Outline each Plasmodium ovale-infected red blood cell.
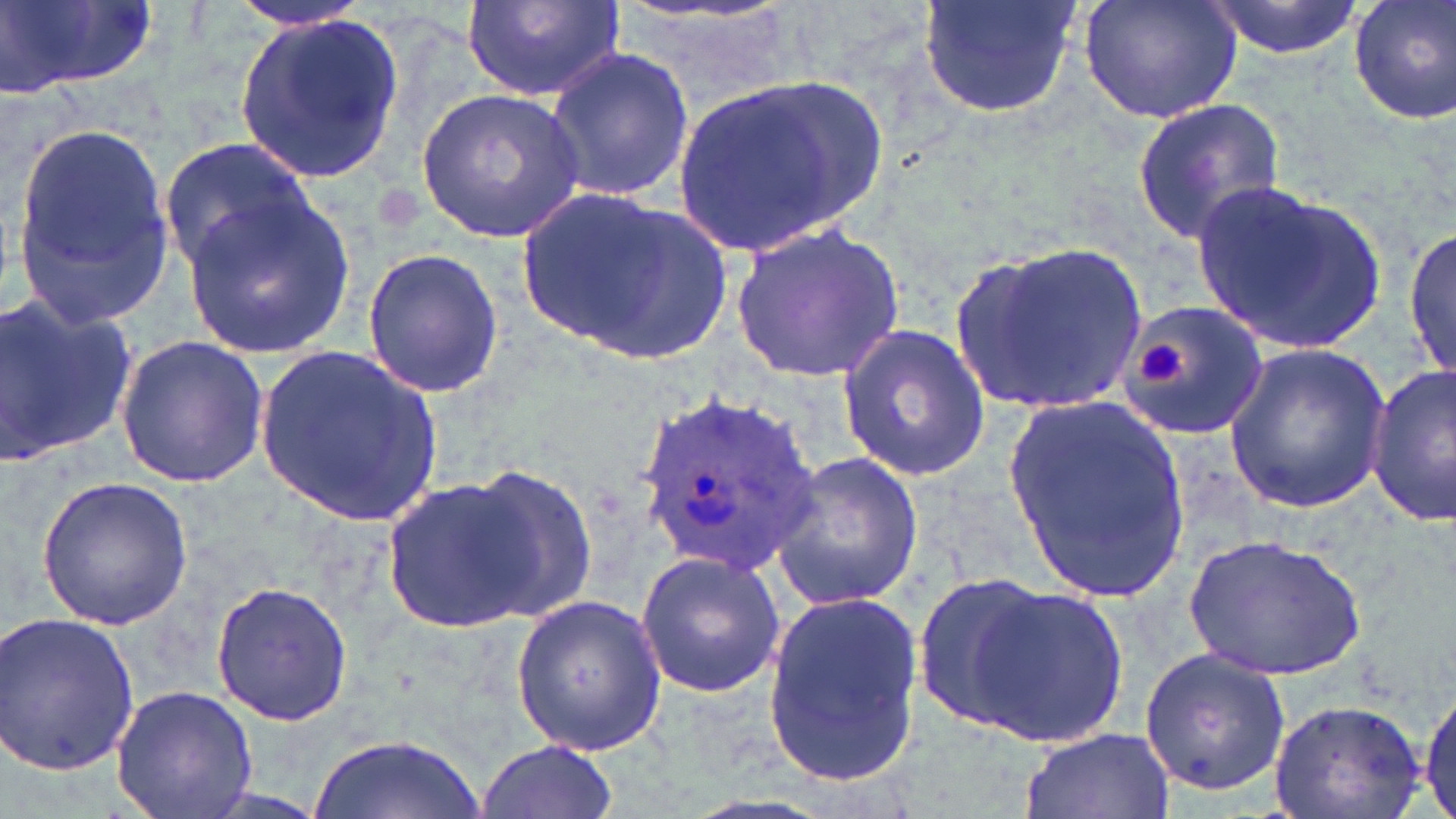

Approximate bounding boxes as [x1, y1, x2, y2] in pixels.
Plasmodium ovale-infected red blood cells: [629, 385, 822, 583].

slide-level diagnosis = Plasmodium ovale
preparation = thin blood smear
platelet locations = approximate bounding boxes as [x1, y1, x2, y2] in pixels: [1138, 341, 1185, 386]
image size = 1456×819 pixels
stain = May-Grünwald-Giemsa
magnification = 1000x
field of view = single
uninfected red blood cell locations = approximate bounding boxes as [x1, y1, x2, y2] in pixels: [4, 0, 156, 98], [227, 0, 373, 33], [460, 0, 625, 104], [916, 0, 1083, 121], [1078, 0, 1244, 125], [1205, 0, 1362, 59], [1349, 0, 1456, 127], [230, 10, 407, 187], [544, 45, 696, 204], [670, 74, 888, 262], [416, 85, 584, 242], [1130, 97, 1287, 245], [10, 120, 180, 321], [159, 138, 312, 274], [1192, 180, 1389, 355], [512, 186, 731, 367], [183, 195, 356, 358], [731, 219, 903, 384], [1404, 226, 1456, 384], [950, 239, 1152, 417], [362, 246, 505, 398], [0, 289, 138, 473], [1116, 302, 1270, 440], [837, 324, 991, 482], [115, 333, 270, 487], [1223, 343, 1393, 515], [257, 346, 443, 528], [1365, 363, 1456, 525], [1005, 393, 1192, 600], [766, 451, 926, 610], [452, 467, 598, 623], [37, 475, 194, 628], [378, 475, 551, 634], [1183, 533, 1365, 681], [633, 550, 788, 698], [911, 574, 1061, 734], [953, 579, 1129, 752], [211, 581, 355, 727], [761, 589, 924, 784], [509, 592, 668, 758], [0, 609, 141, 776], [1138, 647, 1290, 797], [111, 685, 259, 818], [1417, 685, 1454, 816], [1270, 698, 1431, 818], [1018, 726, 1175, 818], [308, 734, 487, 819], [476, 738, 619, 819]
modality = light microscopy